Mark where platelets are.
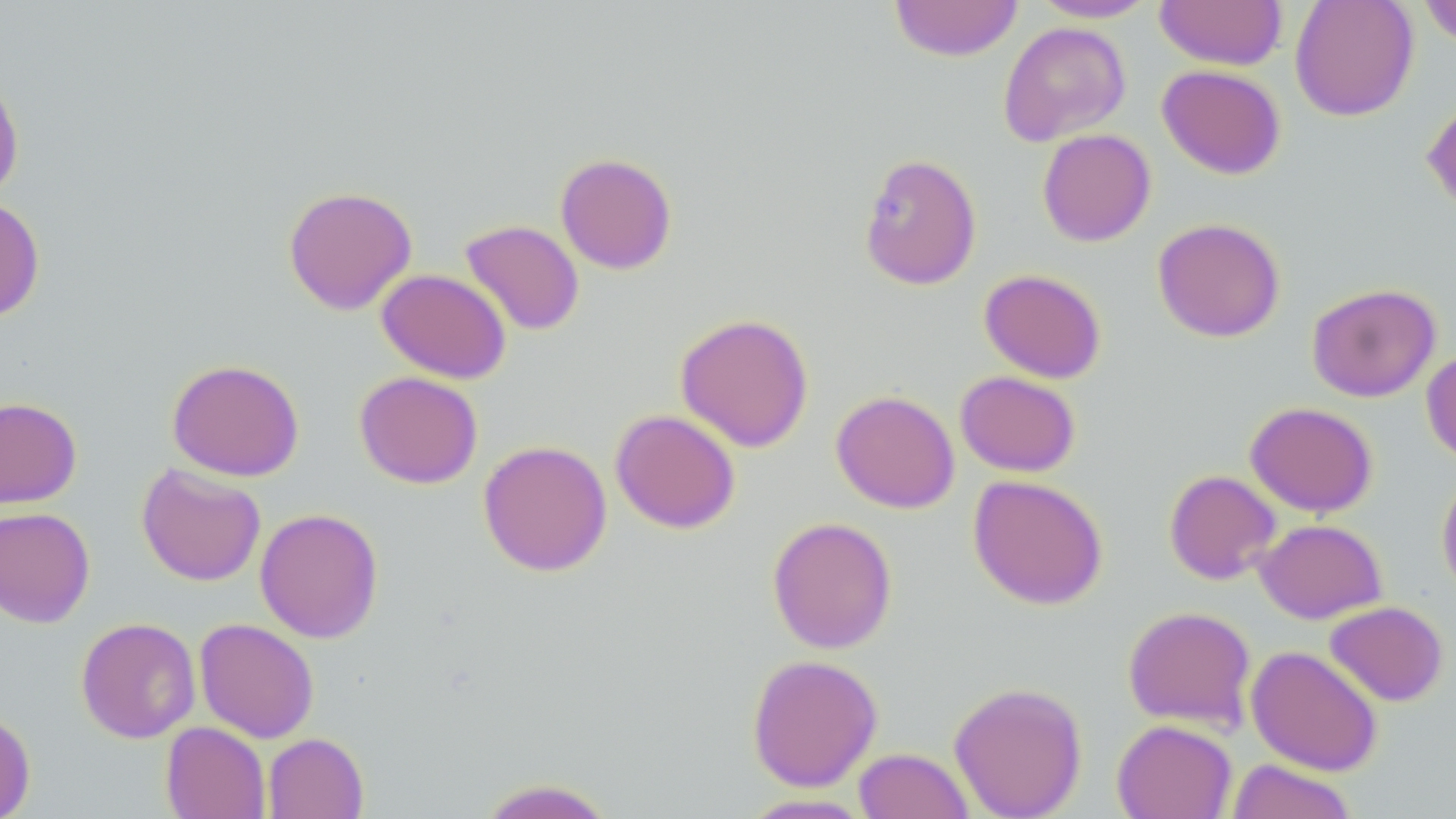
Approximate bounding boxes as (x1,y1)-(x2,y2) corner pairs in pixels.
Platelets: (875,192)-(918,233).

{
  "slide_level_diagnosis": "no evidence of blood parasites",
  "stain": "May-Grünwald-Giemsa",
  "image_size": "1456×819 pixels",
  "preparation": "thin blood film",
  "uninfected_red_blood_cell_locations": "approximate bounding boxes as (x1,y1)-(x2,y2) corner pairs in pixels: (888,0)-(1024,62), (1155,0)-(1286,71), (1289,0)-(1419,121), (1417,0)-(1456,49), (1028,1)-(1160,23), (998,21)-(1131,146), (1157,64)-(1286,179), (0,70)-(24,203), (1421,96)-(1456,216), (1037,129)-(1156,247), (858,152)-(982,290), (555,153)-(677,274), (282,185)-(418,315), (0,196)-(45,323), (1152,217)-(1286,343), (460,219)-(585,336), (376,268)-(511,383), (979,268)-(1107,383), (1306,282)-(1441,403), (675,313)-(814,453), (1421,349)-(1456,465), (166,358)-(304,481), (954,370)-(1081,477), (354,371)-(483,489), (831,389)-(960,513), (0,396)-(82,508), (1245,401)-(1378,517), (610,409)-(741,534), (477,439)-(612,577), (136,463)-(266,586), (1164,469)-(1281,585), (1436,469)-(1456,600), (967,474)-(1109,610), (0,506)-(95,628), (254,507)-(384,644), (767,516)-(897,654), (1254,518)-(1387,623), (1324,600)-(1449,706), (1122,605)-(1257,732), (75,617)-(201,743), (194,618)-(319,743), (1246,645)-(1383,775), (746,653)-(883,791), (948,681)-(1088,819), (0,707)-(36,819), (1111,719)-(1237,818), (160,722)-(270,819), (262,732)-(369,819), (853,747)-(975,819), (1225,759)-(1358,819), (475,778)-(618,819), (738,793)-(876,818)",
  "field_of_view": "single",
  "magnification": "1000x",
  "modality": "optical microscopy"
}